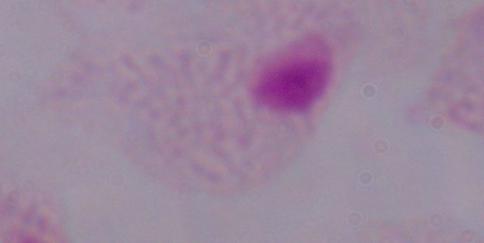
Summary:
  - Modality: micrograph
  - Magnification: 1000x
  - Identification: trichomonad